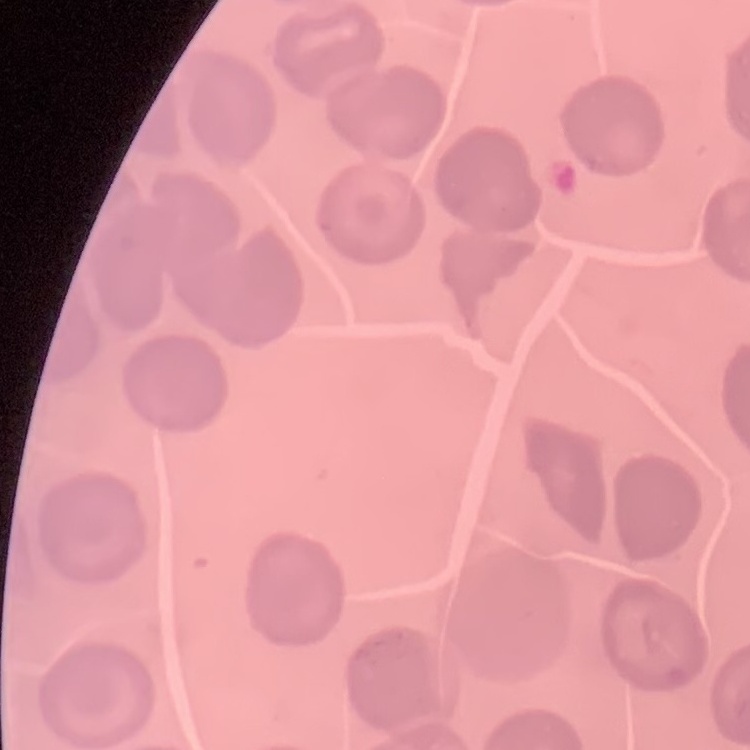
The red blood cells exhibit no rouleaux formation. Square crop of a larger photomicrograph. Field's or Giemsa stain. Thin peripheral smear.